Assess this cell for malaria.
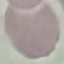
Uninfected.

Summary:
  - Preparation: thin blood smear
  - Stain: Giemsa
  - Capture: smartphone through the microscope eyepiece
  - Image type: cell patch, automatically extracted from a larger field of view and resized to 64 × 64 pixels